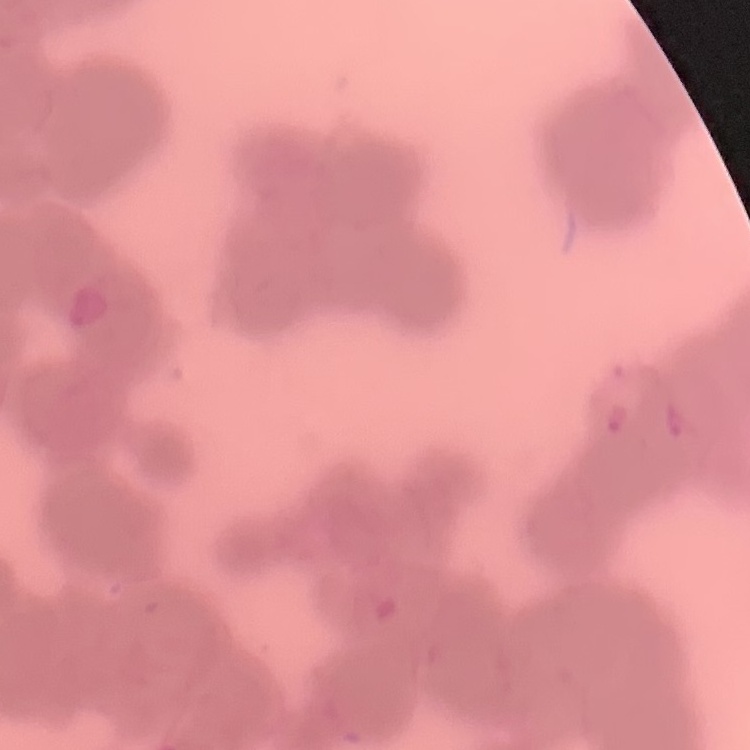
The erythrocytes exhibit rouleaux formation. Square crop of a larger photomicrograph. Field's or Giemsa stain. Thin blood smear.